Outline each blood parasite and name the species.
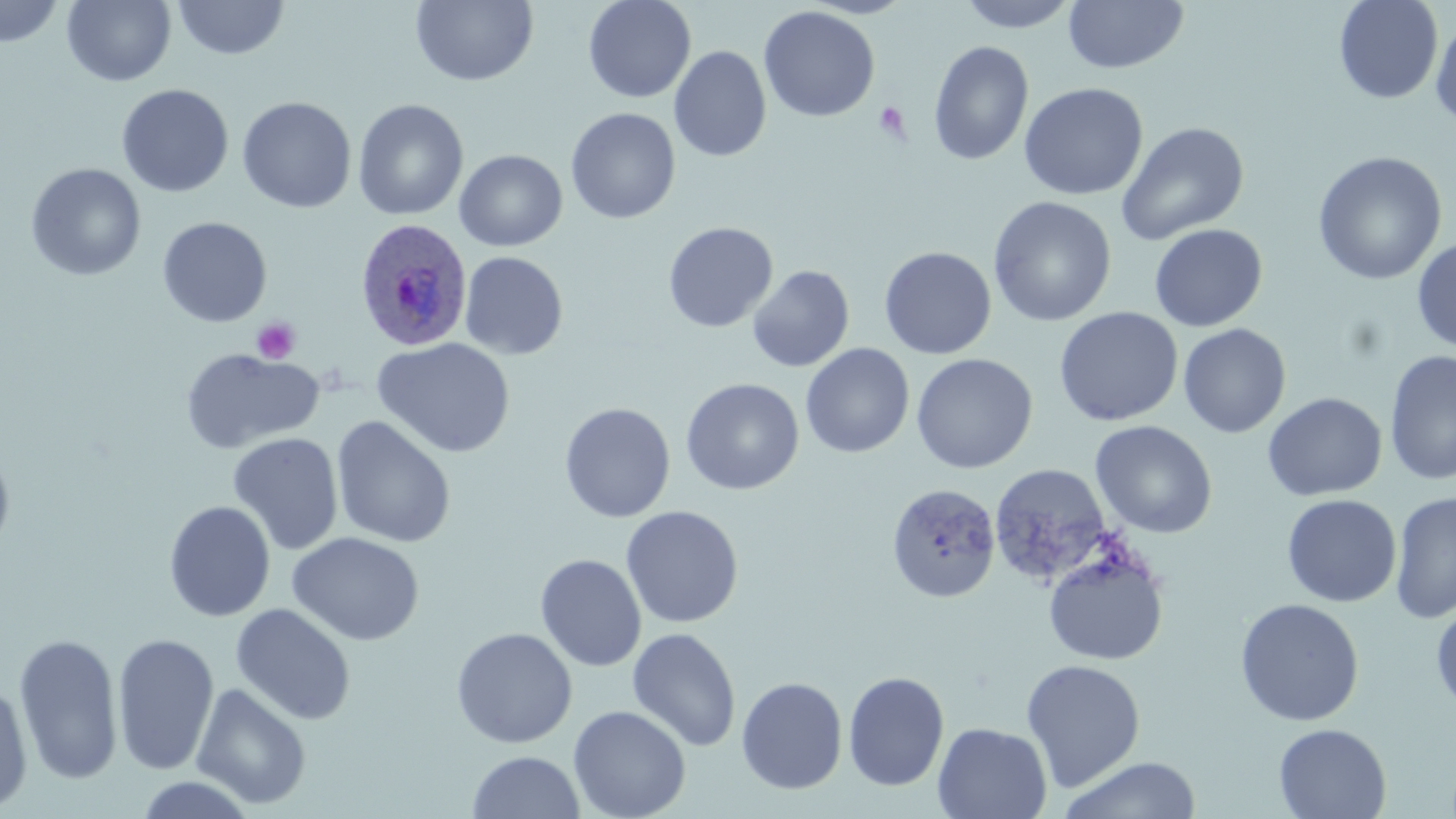
Approximate bounding boxes as named x1/y1/x2/y2 corners in pixels.
Plasmodium ovale-infected red blood cells: (x1=352, y1=217, x2=473, y2=351).
No Plasmodium falciparum, Plasmodium malariae, Plasmodium vivax, Babesia divergens, or Trypanosoma brucei observed.

Summary:
  - Platelet locations: (x1=873, y1=101, x2=912, y2=143), (x1=251, y1=317, x2=300, y2=364)
  - Uninfected red blood cell locations: (x1=62, y1=0, x2=176, y2=86), (x1=173, y1=0, x2=291, y2=61), (x1=583, y1=0, x2=696, y2=103), (x1=800, y1=0, x2=918, y2=19), (x1=955, y1=0, x2=1081, y2=33), (x1=1333, y1=0, x2=1444, y2=104), (x1=0, y1=1, x2=65, y2=48), (x1=411, y1=1, x2=538, y2=87), (x1=1064, y1=1, x2=1189, y2=74), (x1=758, y1=6, x2=880, y2=122), (x1=1430, y1=16, x2=1456, y2=129), (x1=928, y1=41, x2=1033, y2=165), (x1=669, y1=45, x2=771, y2=162), (x1=1019, y1=82, x2=1148, y2=201), (x1=116, y1=83, x2=234, y2=197), (x1=237, y1=97, x2=356, y2=213), (x1=353, y1=98, x2=468, y2=220), (x1=566, y1=108, x2=681, y2=224), (x1=1115, y1=121, x2=1250, y2=245), (x1=454, y1=149, x2=568, y2=251), (x1=1311, y1=151, x2=1448, y2=285), (x1=25, y1=163, x2=147, y2=281), (x1=987, y1=196, x2=1117, y2=327), (x1=157, y1=216, x2=272, y2=327), (x1=663, y1=221, x2=778, y2=333), (x1=1149, y1=224, x2=1268, y2=332), (x1=1412, y1=236, x2=1456, y2=354), (x1=700, y1=242, x2=838, y2=359), (x1=879, y1=246, x2=996, y2=359), (x1=459, y1=251, x2=569, y2=360), (x1=747, y1=265, x2=855, y2=372), (x1=1053, y1=307, x2=1183, y2=427), (x1=1177, y1=323, x2=1291, y2=438), (x1=372, y1=337, x2=516, y2=458), (x1=800, y1=343, x2=915, y2=458), (x1=179, y1=347, x2=325, y2=453), (x1=1384, y1=350, x2=1456, y2=485), (x1=911, y1=353, x2=1038, y2=474), (x1=681, y1=377, x2=804, y2=495), (x1=1263, y1=392, x2=1387, y2=501), (x1=559, y1=402, x2=676, y2=523), (x1=332, y1=415, x2=456, y2=549), (x1=1090, y1=420, x2=1217, y2=539), (x1=228, y1=432, x2=344, y2=555), (x1=0, y1=442, x2=16, y2=564), (x1=988, y1=463, x2=1114, y2=586), (x1=886, y1=482, x2=1001, y2=603), (x1=1389, y1=490, x2=1456, y2=625), (x1=1281, y1=494, x2=1402, y2=607), (x1=164, y1=500, x2=276, y2=622), (x1=620, y1=505, x2=744, y2=628), (x1=288, y1=531, x2=425, y2=646), (x1=1043, y1=542, x2=1170, y2=667), (x1=534, y1=553, x2=647, y2=671), (x1=1235, y1=598, x2=1364, y2=727), (x1=1431, y1=601, x2=1456, y2=715), (x1=231, y1=603, x2=356, y2=725), (x1=451, y1=627, x2=578, y2=748), (x1=627, y1=627, x2=742, y2=752), (x1=14, y1=631, x2=124, y2=785), (x1=112, y1=632, x2=220, y2=776), (x1=1021, y1=659, x2=1146, y2=792), (x1=842, y1=671, x2=949, y2=791), (x1=736, y1=676, x2=848, y2=795), (x1=0, y1=677, x2=34, y2=814), (x1=191, y1=682, x2=312, y2=810), (x1=568, y1=705, x2=692, y2=819), (x1=933, y1=722, x2=1052, y2=819), (x1=1273, y1=723, x2=1391, y2=818), (x1=467, y1=750, x2=585, y2=818), (x1=1057, y1=756, x2=1203, y2=819), (x1=133, y1=774, x2=258, y2=818)
  - Slide-level diagnosis: Plasmodium ovale
  - Preparation: thin blood film
  - Modality: light microscopy
  - Field of view: one of a larger specimen
  - Image size: 1456×819 pixels
  - Magnification: 1000x
  - Stain: May-Grünwald-Giemsa